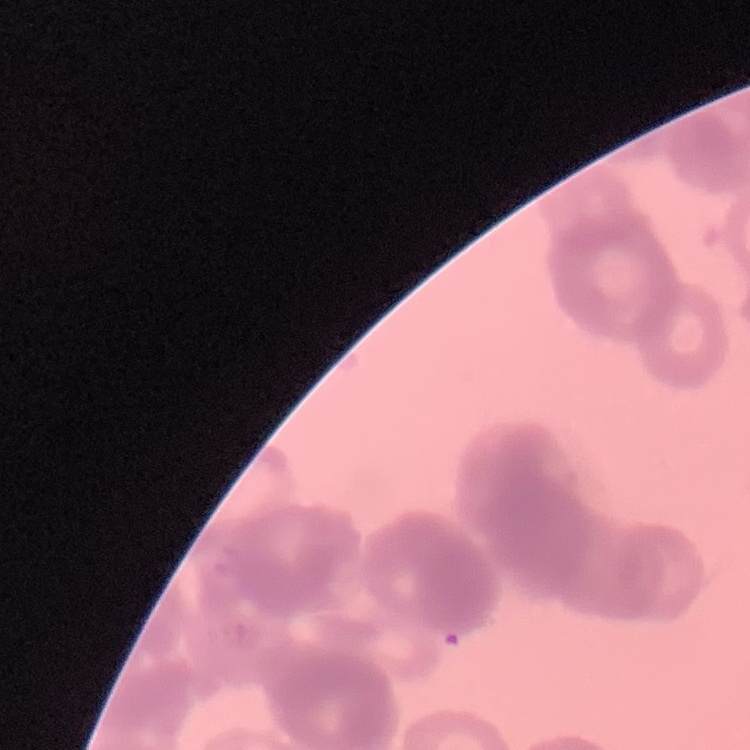

The erythrocytes exhibit rouleaux formation. Thin blood film. Field's or Giemsa stain. One tile cut from a larger photomicrograph.